Report the malaria status of this cell.
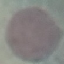

It is uninfected.

capture: smartphone through the microscope eyepiece
stain: Giemsa
preparation: thin blood smear
image_type: automatically extracted cell patch, resized to 64 × 64 pixels